Find the red blood cells that are infected with Plasmodium falciparum, and any of indeterminate infection status.
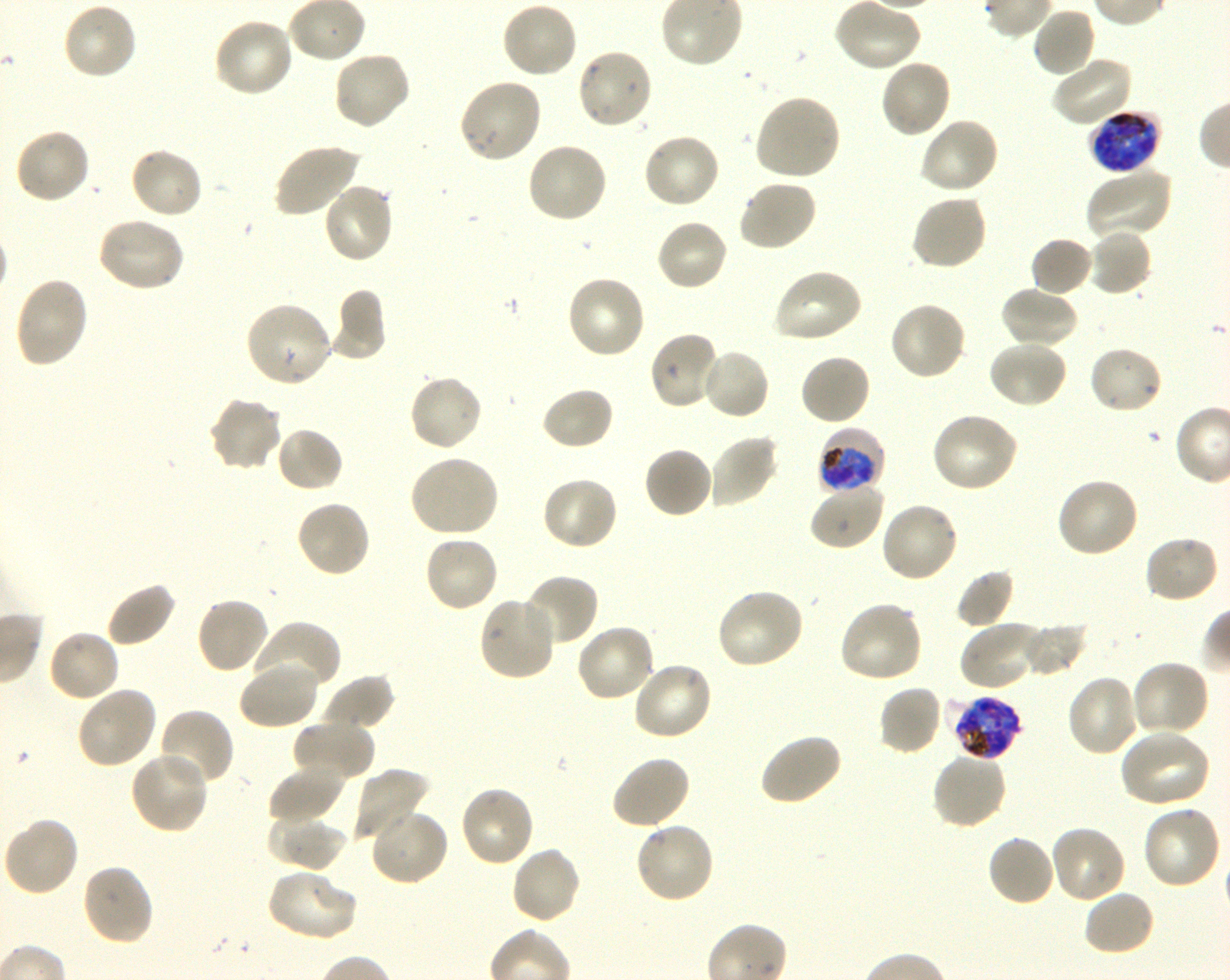

Approximate bounding boxes as [x1, y1, x2, y2] in pixels. Not every red blood cell is marked. A life-cycle stage — or a range of stages, where the recorded stages span more than one — follows each staged infected red blood cell.
Infected red blood cells: [1088, 110, 1162, 175] late trophozoite to late schizont; [817, 426, 885, 496] early trophozoite to early schizont; [952, 695, 1024, 761] late trophozoite to late schizont.
No red blood cells of indeterminate infection status observed.

Locations of uninfected red blood cells: [834, 0, 922, 72], [501, 1, 579, 80], [61, 2, 139, 81], [1032, 7, 1096, 79], [211, 17, 295, 99], [575, 47, 653, 131], [331, 50, 412, 131], [1051, 54, 1133, 128], [879, 58, 954, 139], [458, 76, 543, 164], [753, 94, 841, 182], [919, 117, 1000, 195], [14, 127, 92, 205], [640, 132, 721, 210], [525, 141, 609, 224], [271, 143, 362, 218], [129, 145, 204, 220], [1086, 167, 1172, 241], [737, 179, 818, 253], [321, 181, 395, 264], [910, 192, 988, 271], [96, 216, 186, 294], [656, 217, 729, 293], [1087, 228, 1153, 297], [1030, 237, 1094, 297], [771, 268, 863, 345], [564, 274, 647, 360], [13, 275, 90, 368], [999, 285, 1079, 350], [329, 290, 387, 360], [888, 300, 967, 381], [243, 301, 334, 389], [648, 330, 723, 411], [986, 340, 1068, 410], [1087, 344, 1164, 415], [699, 348, 771, 421], [799, 353, 872, 427], [407, 374, 484, 453], [540, 386, 615, 451], [208, 396, 283, 473], [930, 412, 1019, 494], [274, 425, 345, 494], [708, 434, 779, 508], [643, 446, 714, 519], [407, 454, 500, 538], [541, 476, 619, 551], [1055, 476, 1140, 558], [809, 481, 885, 551], [295, 499, 372, 579], [879, 502, 960, 584], [423, 533, 500, 613], [1142, 534, 1220, 605], [954, 567, 1015, 629], [520, 574, 601, 648], [105, 581, 177, 648], [714, 588, 805, 671], [477, 595, 556, 681], [195, 596, 271, 675], [837, 600, 924, 684], [1019, 620, 1087, 677], [253, 621, 340, 696], [958, 621, 1045, 691], [575, 622, 657, 702], [46, 628, 121, 703], [239, 660, 320, 730], [631, 660, 713, 742], [1131, 660, 1211, 738], [321, 674, 395, 731], [1066, 674, 1142, 757], [877, 684, 944, 756], [76, 686, 158, 770], [156, 708, 235, 790], [292, 720, 375, 783], [1117, 728, 1212, 810], [757, 731, 843, 807], [129, 750, 210, 834], [931, 750, 1008, 830], [611, 754, 692, 829], [267, 764, 345, 824], [351, 768, 430, 845], [459, 785, 535, 869], [1141, 804, 1222, 889], [369, 807, 449, 887], [268, 815, 350, 873], [2, 816, 80, 897], [634, 821, 716, 904], [1049, 824, 1127, 904], [986, 834, 1056, 907], [509, 845, 581, 926], [80, 863, 155, 946], [265, 868, 358, 942], [1083, 889, 1157, 958]. Giemsa-stained preparation. Image is 1230×980 pixels. Thin blood film. Donor blood group O+. One field from this slide. 100x oil-immersion objective, numerical aperture 1.30. Plasmodium falciparum strain 3D7 maintained in shaking in-vitro culture.